Point out leukocytes.
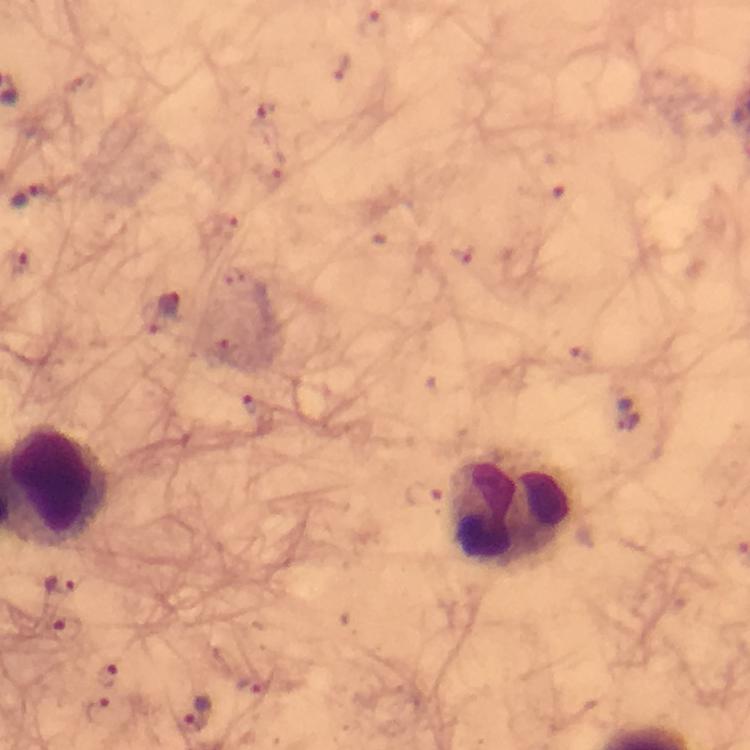
Approximate centers as (x, y) in pixels.
Leukocytes: (58, 487), (513, 513).

Summary:
  - Plasmodium parasite locations: (265, 117), (29, 194), (167, 304), (626, 413), (59, 582), (66, 630), (107, 676), (100, 710), (196, 715)
  - Context: from a diagnostic examination for malaria
  - Preparation: thick smear
  - Stain: Giemsa
  - Capture: smartphone mounted on the microscope
  - Cropped from: one field of view
  - Image size: 750×750 pixels
  - Magnification: 100x
  - Immersion oil: used